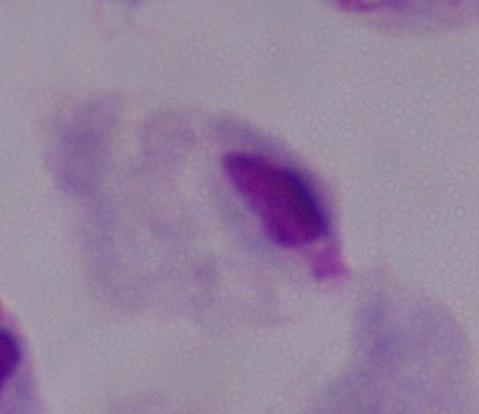
Summary:
  - Identification: trichomonad
  - Magnification: 1000x
  - Modality: photomicrograph